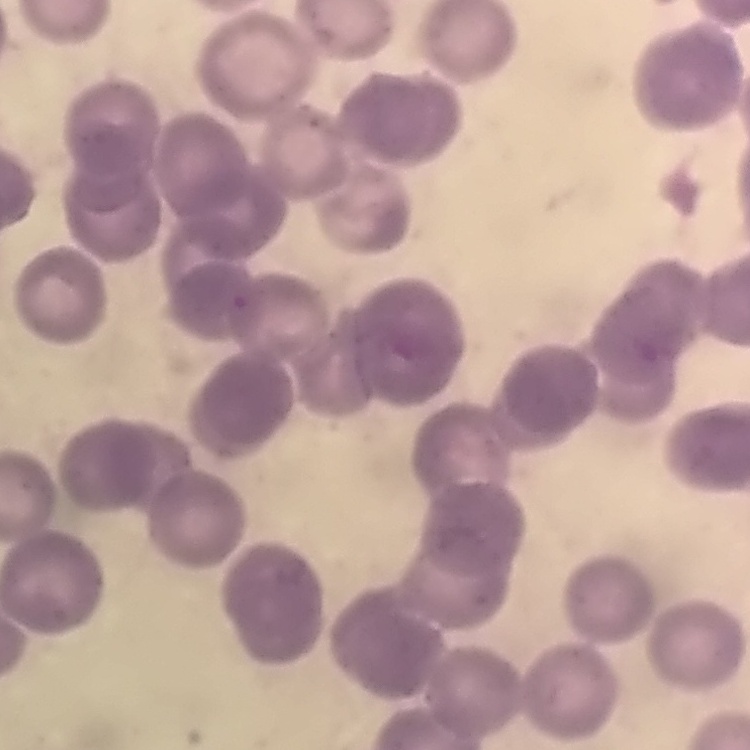
Summary:
  - Red blood cell morphology: rouleaux formation
  - Preparation: thin blood film
  - Stain: Field's or Giemsa
  - Image type: one tile cut from a larger photomicrograph